Classify this cell by malaria status.
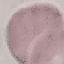

Uninfected.

Summary:
  - Preparation: thin blood smear
  - Capture: smartphone through the microscope eyepiece
  - Stain: Giemsa
  - Image type: automatically extracted cell patch, resized to 64 × 64 pixels